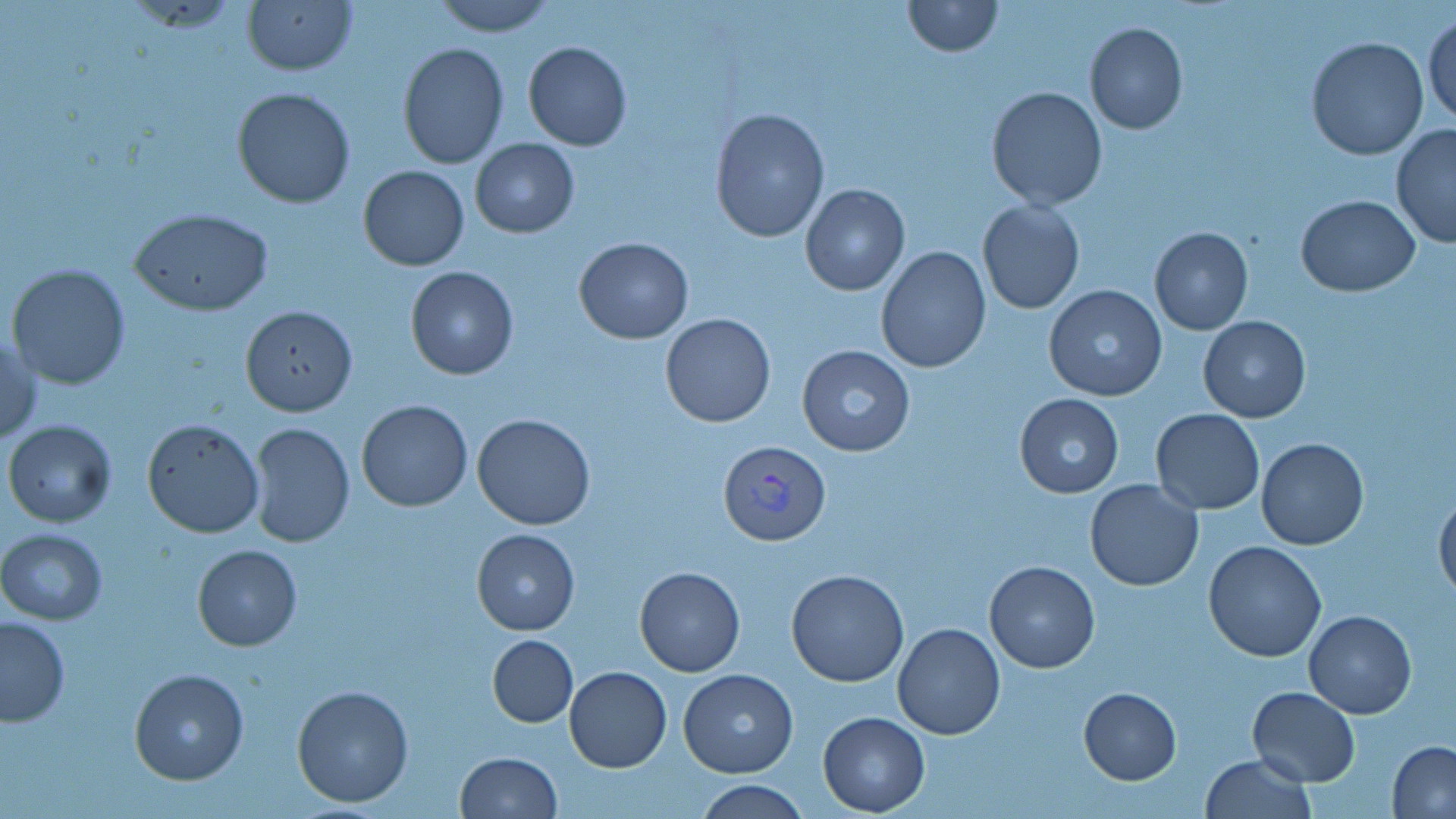

slide_level_diagnosis: Plasmodium vivax
image_size: 1456×819 pixels
magnification: 1000x
preparation: thin blood film
modality: optical microscopy
plasmodium_vivax_infected_red_blood_cell_locations: 'approximate bounding boxes as [x1, y1, x2, y2] in pixels: [719, 439, 829, 547]'
uninfected_red_blood_cell_locations: 'approximate bounding boxes as [x1, y1, x2, y2] in pixels: [429, 0, 559, 37], [900, 0, 1003, 56], [241, 1, 359, 77], [1424, 14, 1456, 130], [1085, 22, 1188, 134], [1306, 36, 1429, 160], [522, 41, 633, 151], [397, 43, 510, 170], [986, 85, 1107, 210], [232, 88, 357, 209], [710, 107, 830, 244], [1390, 124, 1456, 249], [468, 139, 579, 237], [358, 164, 469, 270], [800, 184, 910, 297], [1295, 195, 1421, 295], [977, 200, 1085, 314], [129, 208, 275, 316], [1149, 226, 1254, 335], [574, 237, 693, 344], [875, 245, 992, 373], [6, 263, 130, 391], [405, 266, 519, 380], [1043, 284, 1167, 402], [240, 305, 358, 417], [660, 313, 776, 428], [1197, 316, 1311, 422], [1, 327, 40, 448], [796, 345, 917, 458], [1014, 394, 1124, 497], [357, 399, 472, 512], [1150, 409, 1265, 514], [471, 413, 596, 530], [141, 419, 265, 538], [4, 420, 117, 528], [247, 422, 355, 549], [1257, 439, 1368, 551], [1085, 478, 1204, 592], [1435, 489, 1456, 603], [0, 529, 107, 625], [472, 529, 580, 634], [1204, 540, 1327, 662], [192, 544, 303, 651], [984, 561, 1101, 673], [633, 567, 745, 676], [786, 568, 910, 687], [1303, 610, 1416, 718], [0, 616, 71, 727], [892, 621, 1005, 740], [487, 634, 578, 726], [565, 666, 672, 772], [129, 667, 249, 785], [679, 669, 799, 777], [291, 683, 413, 808], [1078, 686, 1182, 783], [1246, 687, 1360, 786], [818, 712, 929, 815], [1387, 742, 1456, 818], [455, 751, 562, 818], [1201, 754, 1315, 819], [695, 779, 810, 818]'
field_of_view: single
stain: May-Grünwald-Giemsa